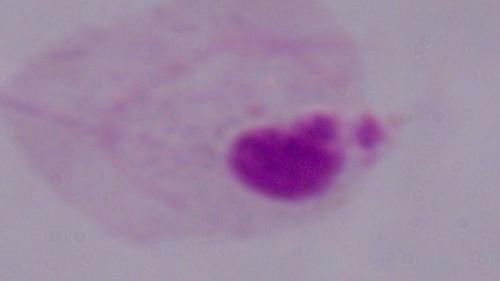
Summary:
  - Identification: trichomonad
  - Modality: micrograph
  - Magnification: 1000x